Outline each blood parasite and name the species.
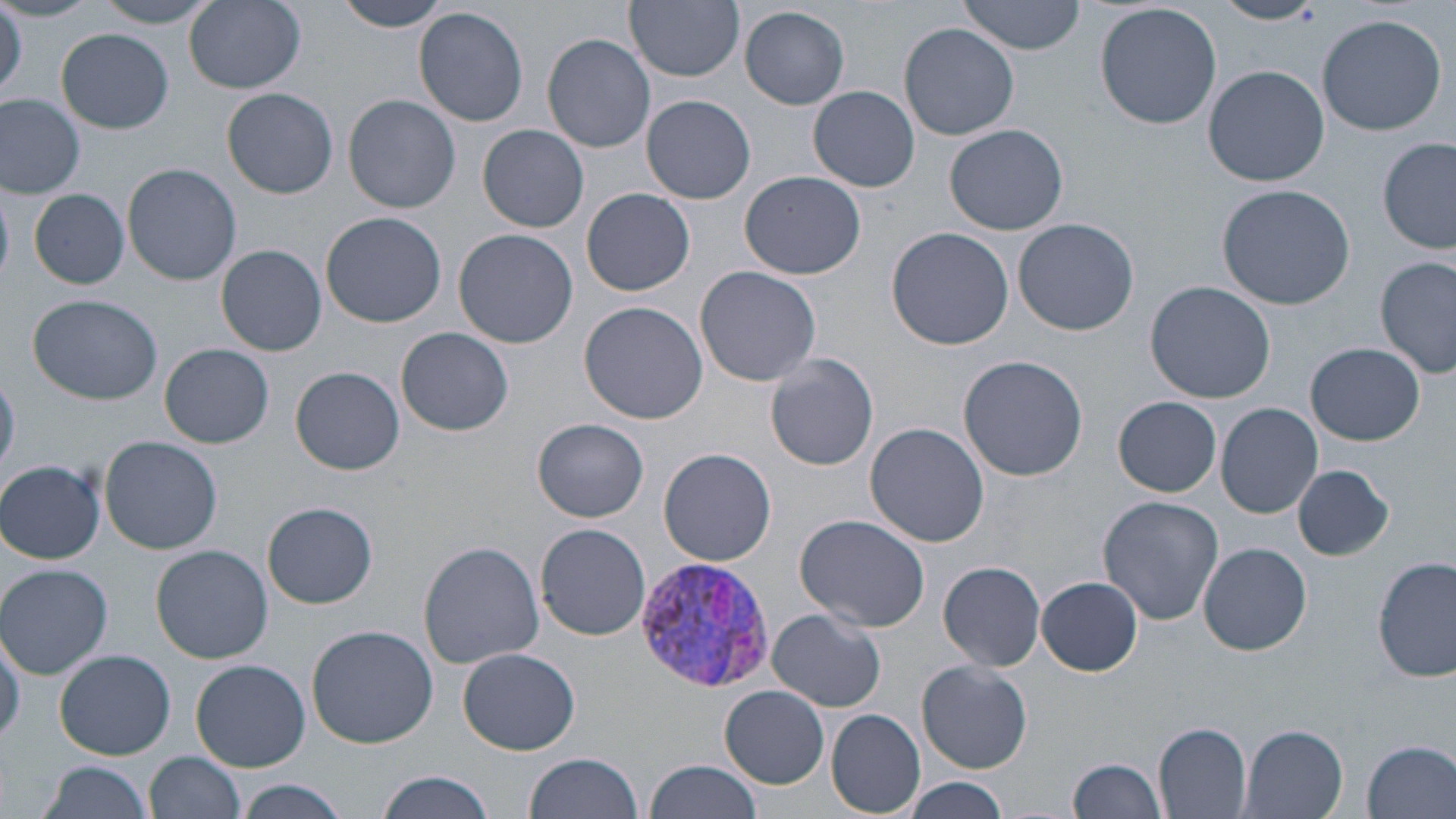
Approximate bounding boxes as (x1,y1)-(x2,y2) corner pairs in pixels.
Plasmodium vivax-infected red blood cells: (629,555)-(775,692).
No Plasmodium falciparum, Plasmodium ovale, Plasmodium malariae, Babesia divergens, or Trypanosoma brucei observed.

slide-level diagnosis = Plasmodium vivax
magnification = 1000x
preparation = thin blood smear
stain = May-Grünwald-Giemsa
uninfected red blood cell locations = approximate bounding boxes as (x1,y1)-(x2,y2) corner pairs in pixels: (0,0)-(96,22), (93,0)-(222,28), (185,0)-(306,93), (334,0)-(450,32), (625,0)-(744,82), (958,1)-(1088,56), (1212,1)-(1324,26), (1095,2)-(1222,131), (0,4)-(25,98), (740,5)-(851,109), (414,7)-(530,128), (1315,13)-(1448,136), (899,24)-(1020,139), (57,29)-(174,134), (541,34)-(656,153), (1203,64)-(1329,186), (376,66)-(519,207), (808,85)-(920,193), (223,88)-(337,199), (0,94)-(86,198), (342,94)-(462,213), (640,94)-(756,204), (945,123)-(1069,236), (478,125)-(588,234), (1377,138)-(1455,253), (122,163)-(242,286), (739,171)-(866,280), (1216,184)-(1356,311), (582,187)-(695,296), (28,188)-(130,289), (321,211)-(447,328), (1013,217)-(1139,336), (886,227)-(1015,351), (454,229)-(579,349), (217,245)-(327,356), (1376,254)-(1455,379), (694,266)-(821,387), (1145,281)-(1276,404), (29,292)-(163,405), (580,302)-(706,424), (396,327)-(514,436), (1306,343)-(1425,446), (161,344)-(273,449), (765,353)-(879,471), (958,355)-(1089,481), (292,365)-(405,475), (0,375)-(21,478), (1111,396)-(1224,496), (1216,403)-(1322,518), (532,418)-(649,522), (865,422)-(988,547), (99,435)-(223,554), (659,448)-(776,566), (0,459)-(105,563), (1293,463)-(1395,561), (1097,495)-(1224,626), (262,502)-(378,609), (795,515)-(932,633), (535,522)-(652,640), (419,541)-(546,669), (1197,542)-(1314,655), (152,545)-(273,663), (1373,555)-(1455,683), (939,560)-(1048,672), (0,562)-(113,679), (1037,577)-(1143,676), (766,610)-(886,713), (0,625)-(24,747), (308,626)-(440,749), (456,647)-(580,755), (55,649)-(175,760), (191,658)-(311,771), (918,660)-(1032,774), (720,685)-(830,789), (827,709)-(925,816), (1154,723)-(1252,817), (1239,725)-(1350,819), (1361,740)-(1455,819), (147,752)-(244,818), (523,754)-(645,819), (1068,758)-(1167,817), (646,759)-(763,819), (38,760)-(155,819), (377,770)-(499,819), (901,778)-(1010,818), (231,780)-(351,819)
image size = 1456×819 pixels
modality = optical microscopy
field of view = one of a larger specimen